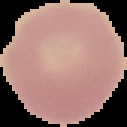

Summary:
  - Image type: segmented cell region with the area outside set to black
  - Result: no Plasmodium parasites detected
  - Image size: 127×127 pixels
  - Preparation: thin blood smear